Classify this cell by malaria status.
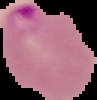

It is parasitized.

From a thin blood smear. Image is 97×100 pixels. Segmented cell region on a black background.